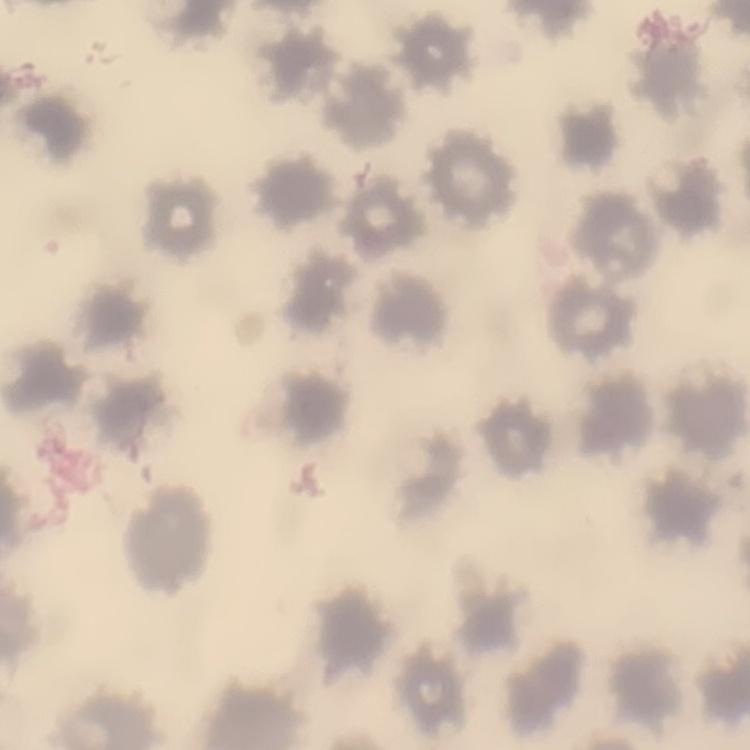

red_blood_cell_morphology: no rouleaux formation
stain: Field's or Giemsa
preparation: thin blood film
image_type: square crop of a larger photomicrograph